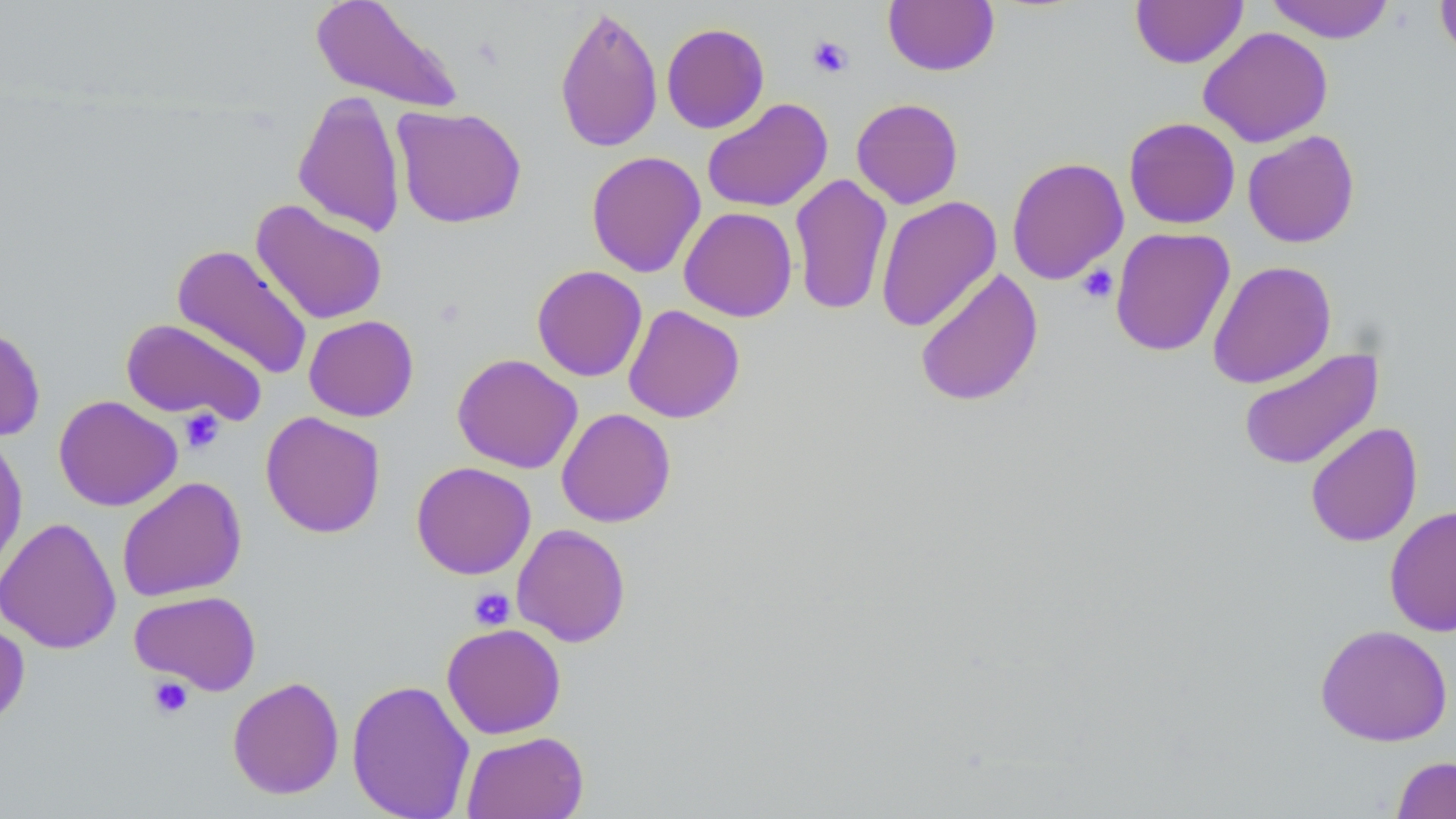

Summary:
  - Coordinate format: approximate bounding boxes as [x1, y1, x2, y2] in pixels
  - Uninfected red blood cell locations: [309, 0, 464, 113], [1265, 0, 1396, 43], [1435, 0, 1456, 63], [883, 1, 999, 75], [1131, 1, 1248, 68], [554, 4, 663, 154], [661, 22, 770, 133], [1198, 26, 1333, 148], [292, 90, 407, 238], [701, 97, 833, 213], [851, 97, 963, 209], [391, 105, 527, 229], [1123, 117, 1240, 229], [1242, 130, 1360, 248], [586, 150, 706, 278], [1006, 156, 1129, 285], [789, 173, 893, 317], [876, 195, 1002, 332], [250, 199, 388, 325], [679, 206, 798, 322], [1110, 227, 1236, 357], [171, 243, 313, 380], [1207, 260, 1337, 389], [531, 265, 647, 381], [914, 267, 1044, 408], [623, 304, 745, 423], [304, 315, 418, 421], [121, 318, 267, 425], [0, 324, 46, 441], [1237, 346, 1384, 472], [452, 353, 582, 473], [53, 395, 182, 511], [556, 408, 675, 527], [260, 411, 386, 538], [1305, 421, 1423, 548], [0, 430, 28, 582], [411, 461, 536, 579], [116, 476, 247, 602], [1385, 505, 1456, 637], [0, 516, 122, 654], [511, 523, 631, 647], [129, 590, 262, 695], [0, 616, 30, 730], [441, 623, 566, 739], [1315, 624, 1453, 746], [227, 676, 345, 799], [346, 678, 475, 819], [460, 731, 589, 819], [1391, 755, 1456, 818]
  - Platelet locations: [807, 36, 853, 78], [1076, 264, 1118, 304], [178, 408, 225, 454], [468, 587, 515, 631], [148, 676, 194, 719]
  - Slide-level diagnosis: negative for blood parasites
  - Field of view: one of a larger specimen
  - Modality: optical microscopy
  - Magnification: 1000x
  - Preparation: thin blood film
  - Image size: 1456×819 pixels
  - Stain: May-Grünwald-Giemsa